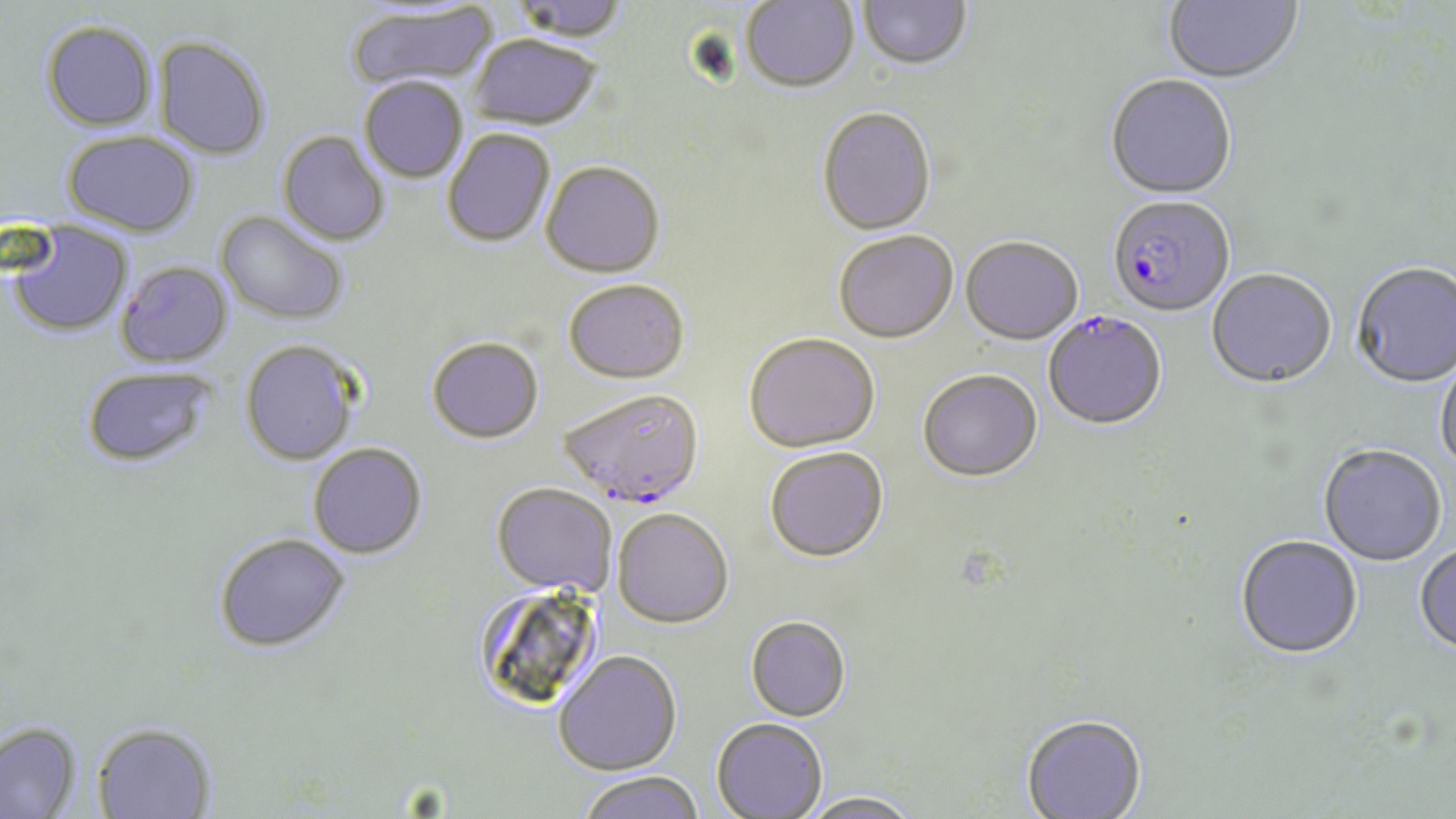
slide-level diagnosis = Plasmodium falciparum
field of view = single
image size = 1456×819 pixels
Plasmodium falciparum-infected red blood cell locations = approximate bounding boxes as named x1/y1/x2/y2 corners in pixels: (x1=1108, y1=197, x2=1235, y2=319), (x1=1043, y1=311, x2=1167, y2=432), (x1=559, y1=391, x2=705, y2=511)
stain = May-Grünwald-Giemsa
preparation = thin blood smear
modality = optical microscopy
uninfected red blood cell locations = approximate bounding boxes as named x1/y1/x2/y2 corners in pixels: (x1=510, y1=0, x2=630, y2=43), (x1=740, y1=0, x2=859, y2=94), (x1=1163, y1=0, x2=1302, y2=85), (x1=856, y1=1, x2=972, y2=73), (x1=347, y1=4, x2=498, y2=91), (x1=40, y1=21, x2=157, y2=132), (x1=467, y1=36, x2=602, y2=132), (x1=153, y1=38, x2=270, y2=162), (x1=1104, y1=75, x2=1236, y2=200), (x1=359, y1=78, x2=468, y2=184), (x1=817, y1=109, x2=937, y2=237), (x1=442, y1=130, x2=555, y2=249), (x1=63, y1=132, x2=199, y2=238), (x1=277, y1=132, x2=390, y2=246), (x1=541, y1=164, x2=665, y2=281), (x1=215, y1=212, x2=348, y2=327), (x1=5, y1=222, x2=132, y2=338), (x1=834, y1=232, x2=958, y2=345), (x1=960, y1=238, x2=1083, y2=346), (x1=115, y1=262, x2=233, y2=368), (x1=1351, y1=263, x2=1456, y2=390), (x1=1207, y1=270, x2=1337, y2=390), (x1=563, y1=282, x2=689, y2=386), (x1=744, y1=334, x2=880, y2=455), (x1=426, y1=339, x2=544, y2=446), (x1=240, y1=341, x2=362, y2=465), (x1=1435, y1=358, x2=1456, y2=477), (x1=81, y1=366, x2=217, y2=469), (x1=917, y1=370, x2=1042, y2=484), (x1=308, y1=444, x2=427, y2=560), (x1=1318, y1=446, x2=1447, y2=567), (x1=765, y1=448, x2=889, y2=564), (x1=490, y1=484, x2=613, y2=597), (x1=612, y1=509, x2=734, y2=630), (x1=214, y1=534, x2=351, y2=655), (x1=1235, y1=536, x2=1363, y2=661), (x1=1414, y1=544, x2=1456, y2=658), (x1=473, y1=583, x2=603, y2=713), (x1=745, y1=616, x2=850, y2=722), (x1=553, y1=651, x2=682, y2=775), (x1=1020, y1=715, x2=1148, y2=819), (x1=711, y1=717, x2=828, y2=818), (x1=0, y1=721, x2=82, y2=819), (x1=92, y1=723, x2=217, y2=819), (x1=577, y1=771, x2=705, y2=819), (x1=800, y1=790, x2=924, y2=819)
magnification = 1000x